Assess for Plasmodium parasites.
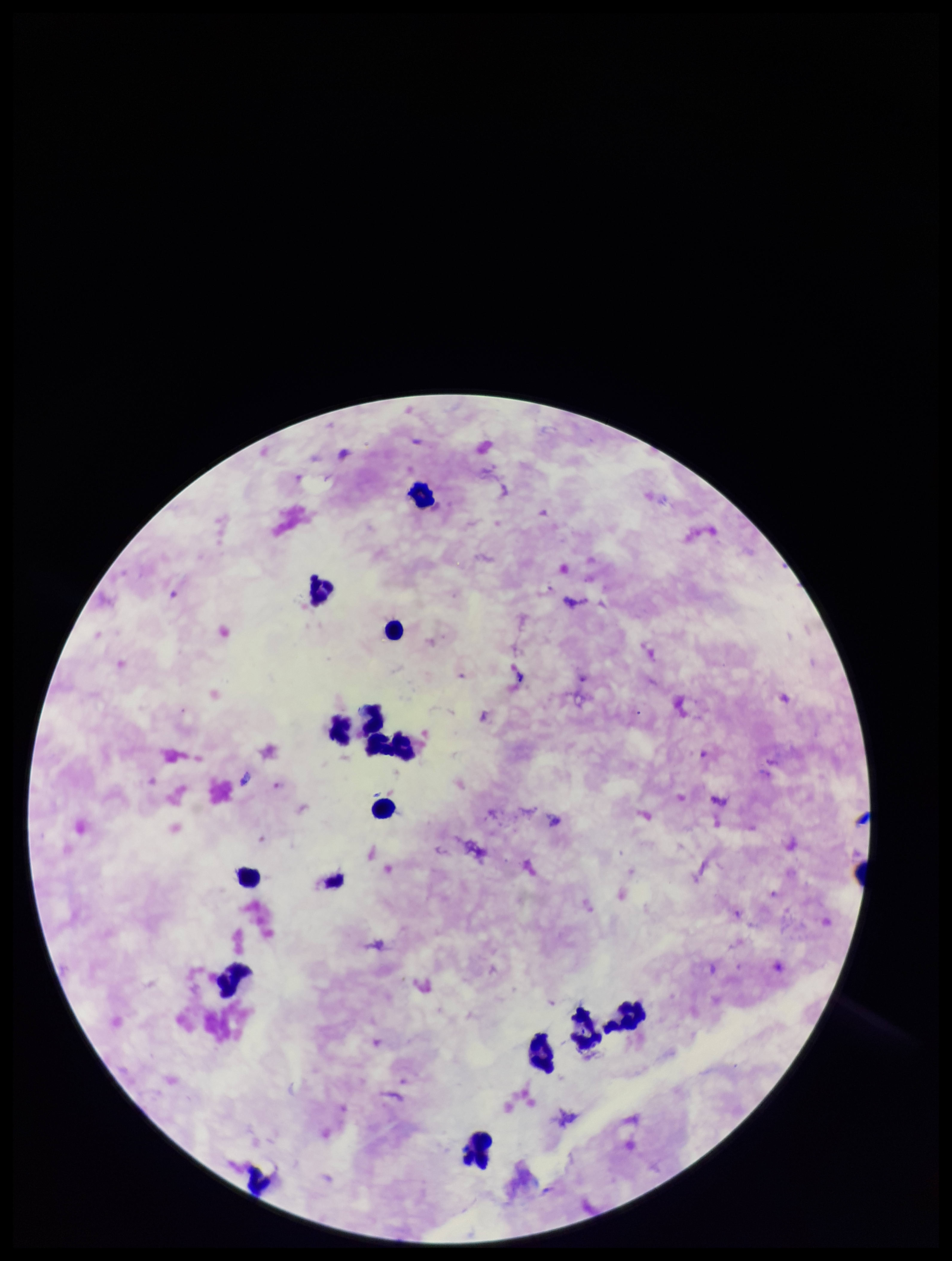
Identified.

capture: smartphone photograph through the microscope eyepiece
image_size: 952×1261 pixels
preparation: thick smear
patient_malaria_status: positive
parasite_count: 2
species_reported_for_this_patient: Plasmodium falciparum
stain: Giemsa
field_of_view: one from this slide
leukocyte_count: 14